Assess for malaria.
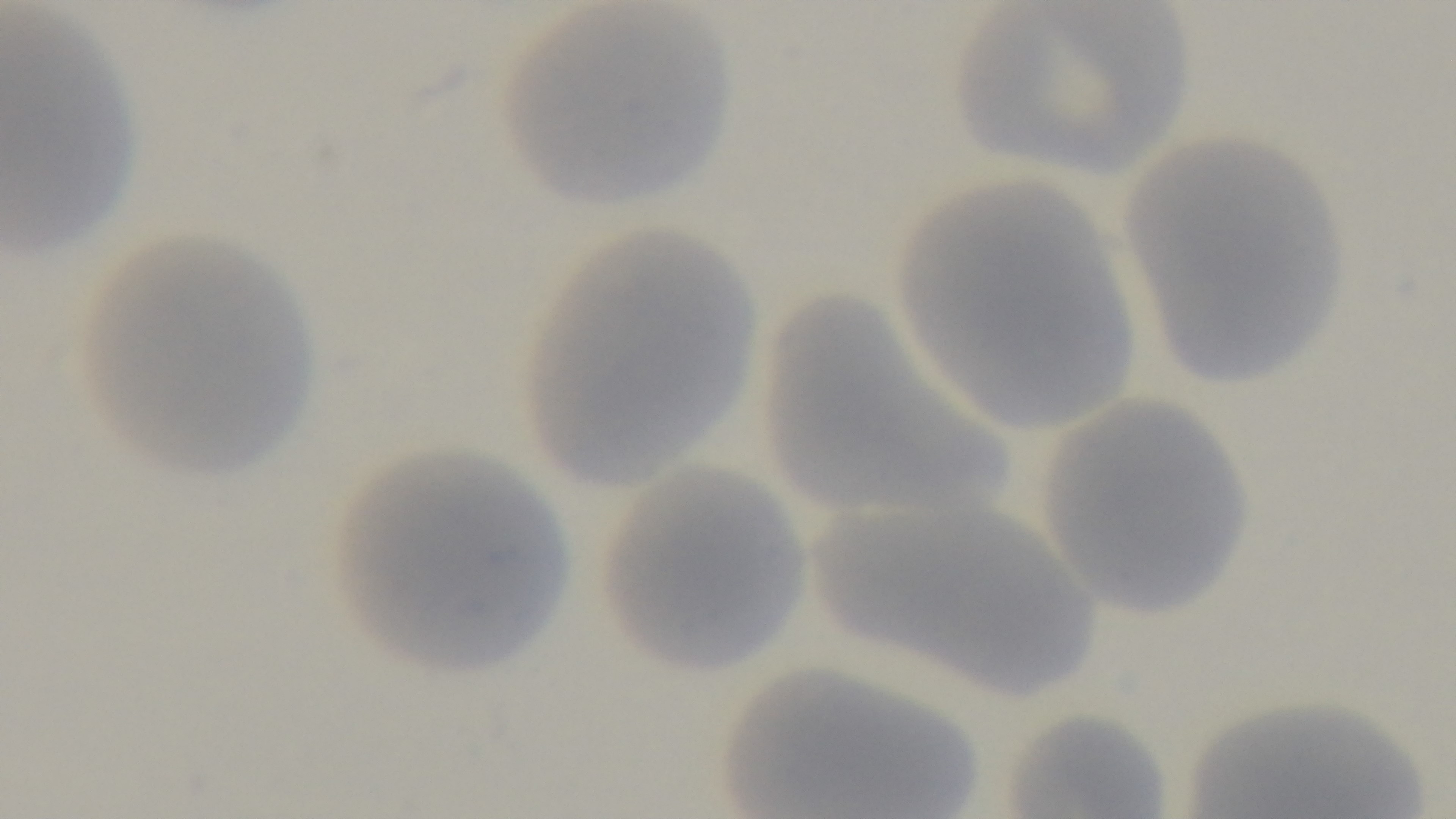

Uninfected.

Summary:
  - Modality: light microscopy
  - Stain: Giemsa
  - Capture: mounted 4K digital camera
  - Field of view: one from the slide
  - Preparation: thin smear
  - Objective: 100x oil immersion